Comment on the morphology of the red blood cells.
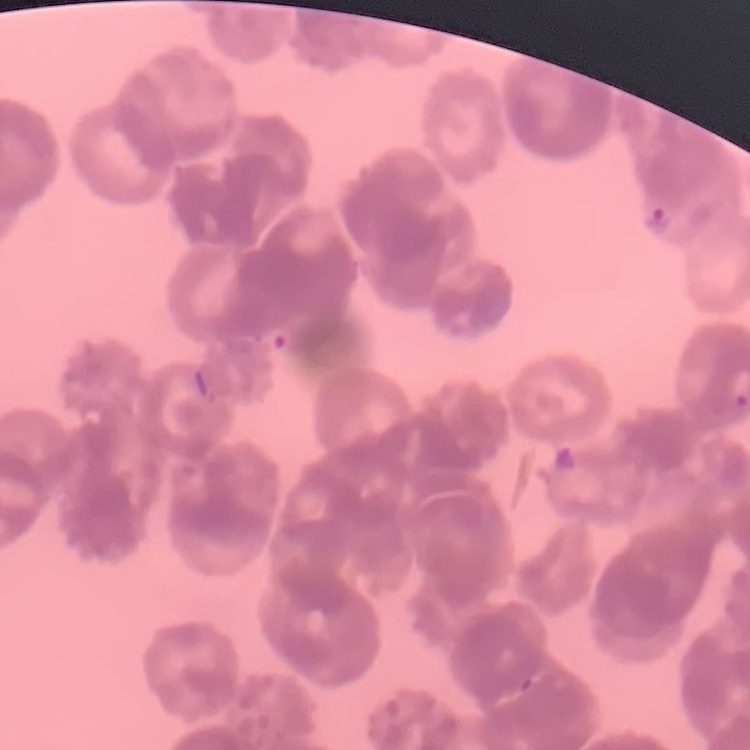
They show rouleaux formation.

Square crop of a larger photomicrograph. Field's or Giemsa stain. Thin blood film.